Name the parasite shown.
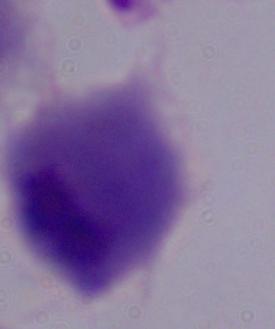

This is a trichomonad.

{
  "magnification": "1000x",
  "modality": "photomicrograph"
}